Report the malaria status of this cell.
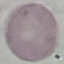
Uninfected.

Photographed with a smartphone camera at the microscope eyepiece. Giemsa-stained preparation. Automatically extracted cell patch, resized to 64 × 64 pixels. Thin blood smear.